Locate every Plasmodium falciparum parasite and identify its life-cycle stage.
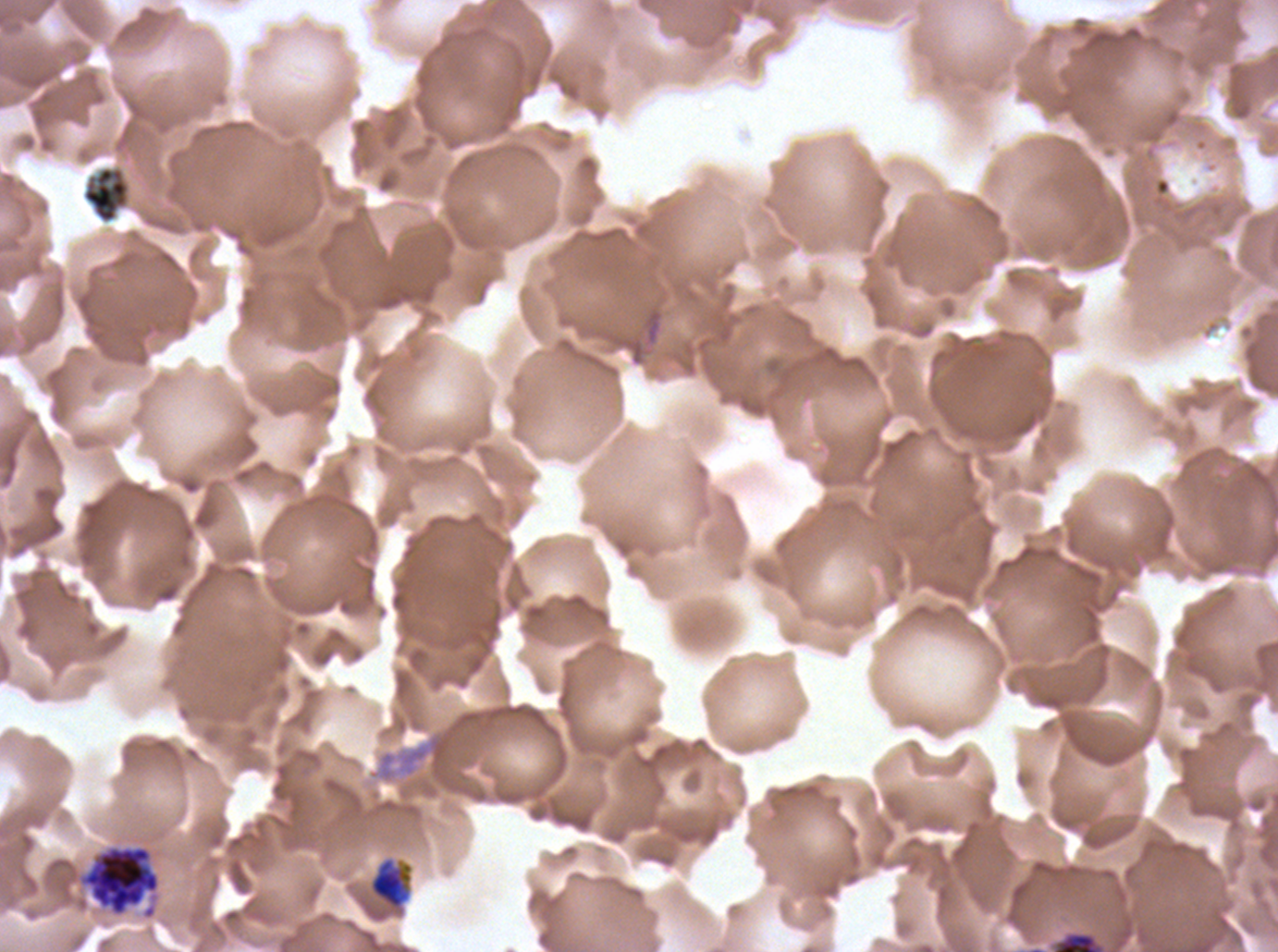
Approximate bounding rectangles given as corner coordinates in pixels from the top-left.
Late trophozoites: (x1=369, y1=858, x2=413, y2=909).
Late schizonts: (x1=76, y1=844, x2=162, y2=921).
No rings, late-ring/early-trophozoite forms, mid trophozoites, early schizonts, segmenters, or gametocytes observed.

specimen: Plasmodium falciparum cultured ex vivo for 24 to 48 hours, from a patient in The Gambia
life_cycle_stages_observed: late trophozoite, late schizont
stain: Giemsa
field_of_view: one sub-image of a larger composite
preparation: thin blood smear
debris_locations: 'approximate bounding rectangles given as corner coordinates in pixels from the top-left: (x1=81, y1=165, x2=131, y2=225), (x1=1053, y1=932, x2=1100, y2=951)'
image_size: 1278×952 pixels